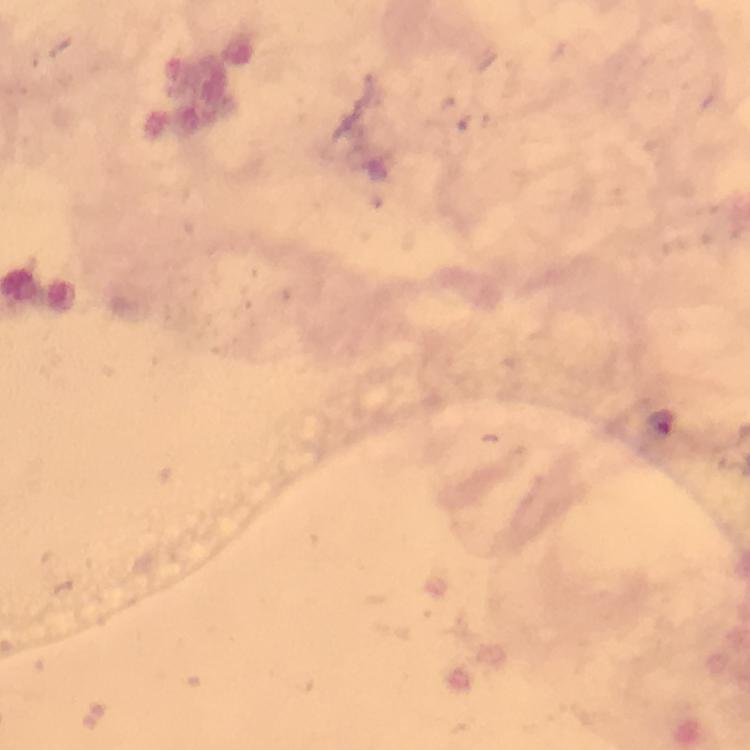
Approximate centers as (x, y) in pixels. Plasmodium parasite locations: (661, 423). At 100x magnification. Thick blood film. Giemsa stain. Immersion oil was used. From a malaria diagnostic workup. A crop from one field of view. Image is 750×750 pixels. Smartphone photograph taken through a microscope.